Classify this cell by malaria status.
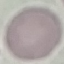
It is uninfected.

Summary:
  - Stain: Giemsa
  - Preparation: thin smear
  - Capture: smartphone through the microscope eyepiece
  - Image type: automatically extracted cell patch, resized to 64 × 64 pixels